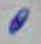
Summary:
  - Magnification: 1000x
  - Modality: photomicrograph
  - Identification: Toxoplasma gondii